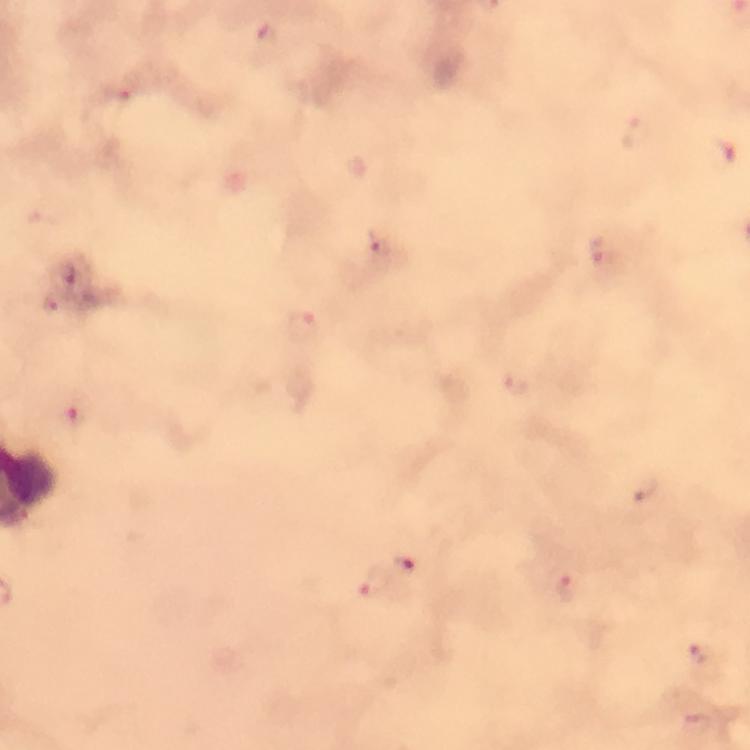

Approximate centers as [x, y] in pixels.
Summary:
  - Plasmodium parasite locations: [267, 39], [118, 93], [636, 132], [376, 244], [599, 250], [52, 303], [303, 327], [516, 384], [77, 414], [643, 488], [406, 564], [375, 579], [567, 587], [699, 654]
  - Context: from a diagnostic examination for malaria
  - Stain: Giemsa
  - Image size: 750×750 pixels
  - Preparation: thick blood smear
  - Cropped from: a single field of view
  - Magnification: 100x
  - Capture: smartphone photograph through a microscope
  - Immersion oil: used